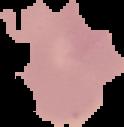

Summary:
  - Image type: segmented cell region with the area outside set to black
  - Preparation: thin blood smear
  - Image size: 124×127 pixels
  - Malaria status: uninfected